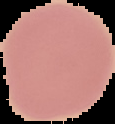
Summary:
  - Malaria status: uninfected
  - Preparation: thin blood film
  - Image type: cell region segmented out of the field of view; surrounding area masked to black
  - Image size: 115×124 pixels